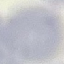
{
  "result": "no malaria parasites detected",
  "image_type": "automatically extracted cell patch, resized to 64 × 64 pixels",
  "capture": "smartphone through the microscope eyepiece",
  "stain": "Giemsa",
  "preparation": "thin blood film"
}